Locate every Babesia divergens-infected red blood cell.
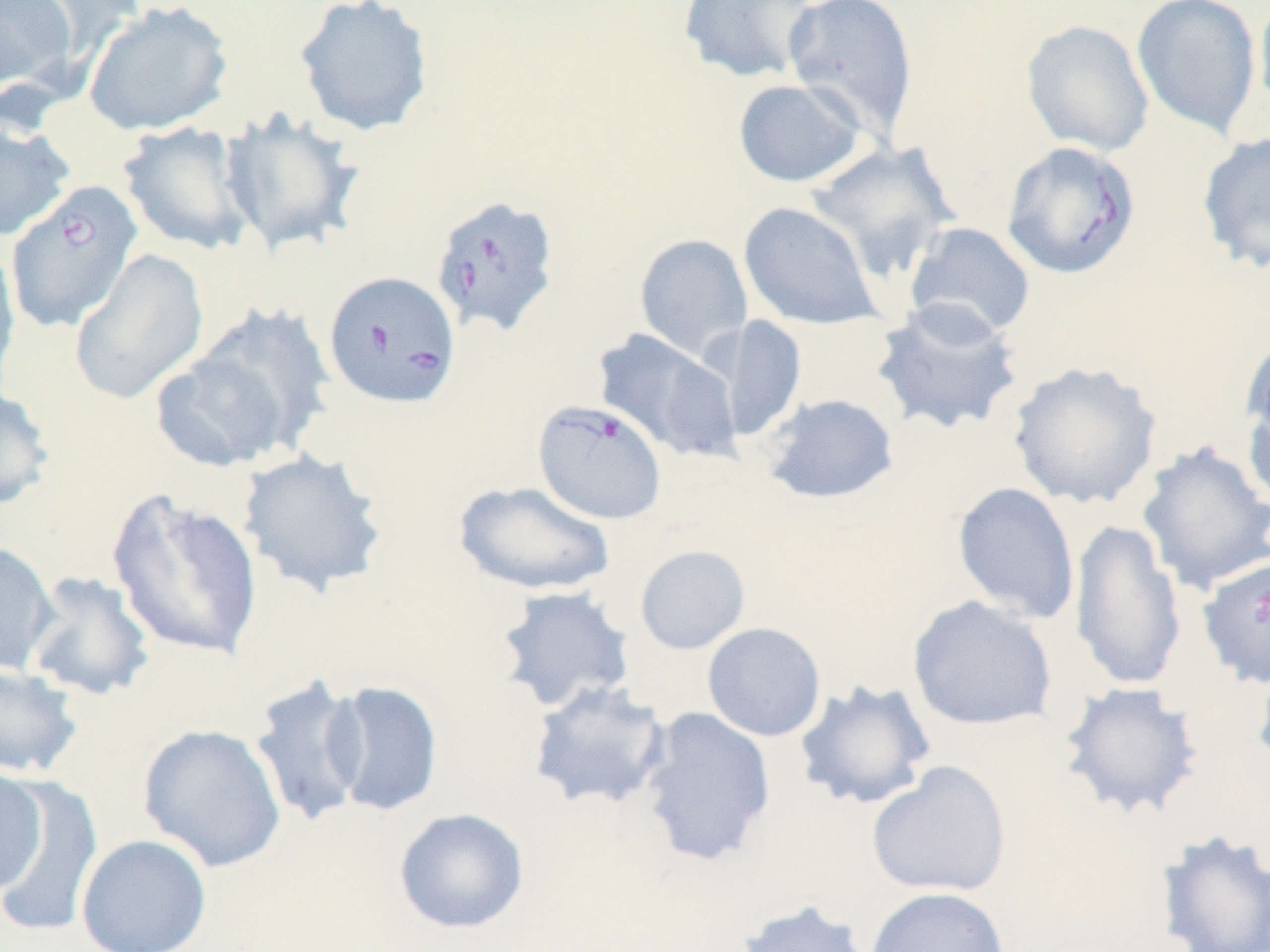

Approximate bounding boxes as [x1, y1, x2, y2] in pixels.
Babesia divergens-infected red blood cells: [1001, 140, 1141, 279], [4, 180, 143, 334], [430, 195, 561, 337], [322, 270, 461, 411], [532, 400, 667, 524], [1197, 555, 1270, 689].

slide-level diagnosis = Babesia divergens
stain = May-Grünwald-Giemsa
uninfected red blood cell locations = approximate bounding boxes as [x1, y1, x2, y2] in pixels: [0, 0, 75, 92], [16, 0, 146, 68], [292, 0, 436, 138], [782, 0, 919, 140], [1131, 0, 1262, 139], [1253, 0, 1270, 119], [82, 1, 234, 137], [678, 1, 819, 84], [1020, 19, 1154, 157], [732, 77, 866, 188], [219, 110, 366, 257], [0, 114, 75, 243], [117, 121, 256, 256], [1197, 131, 1270, 273], [805, 140, 959, 284], [738, 201, 882, 330], [904, 221, 1036, 341], [634, 233, 753, 361], [0, 239, 20, 389], [68, 248, 209, 406], [870, 298, 1025, 438], [190, 303, 336, 456], [710, 315, 808, 442], [593, 327, 743, 462], [1239, 340, 1270, 509], [148, 350, 291, 473], [1007, 360, 1163, 510], [0, 385, 56, 511], [760, 392, 900, 505], [1136, 440, 1270, 595], [237, 448, 390, 599], [453, 480, 616, 596], [952, 481, 1081, 624], [106, 489, 265, 661], [1069, 518, 1187, 692], [0, 541, 59, 677], [634, 545, 751, 655], [23, 570, 156, 702], [493, 585, 636, 714], [907, 595, 1058, 731], [702, 622, 827, 742], [1252, 651, 1270, 783], [0, 663, 84, 778], [247, 673, 372, 828], [793, 678, 937, 811], [528, 679, 671, 811], [324, 680, 444, 818], [1058, 680, 1203, 821], [637, 705, 777, 868], [137, 723, 287, 873], [867, 760, 1012, 898], [0, 764, 49, 898], [0, 776, 102, 937], [393, 807, 530, 935], [1154, 828, 1270, 952], [76, 833, 212, 952], [865, 885, 1011, 952], [735, 899, 876, 952]
preparation = thin blood smear
modality = optical microscopy
image size = 1270×952 pixels
field of view = one of a larger specimen
magnification = 1000x